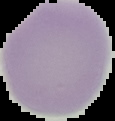
Summary:
  - Image type: segmented cell region on a black background
  - Image size: 115×121 pixels
  - Malaria status: uninfected
  - Preparation: thin blood smear